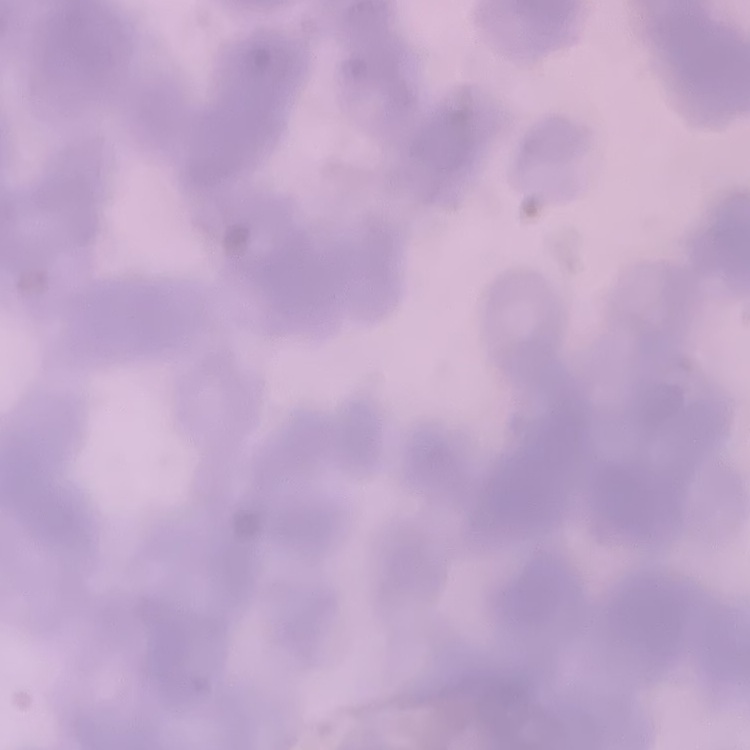

The red blood cells exhibit rouleaux formation. Field's or Giemsa stain. Thin blood smear. One tile cut from a larger photomicrograph.